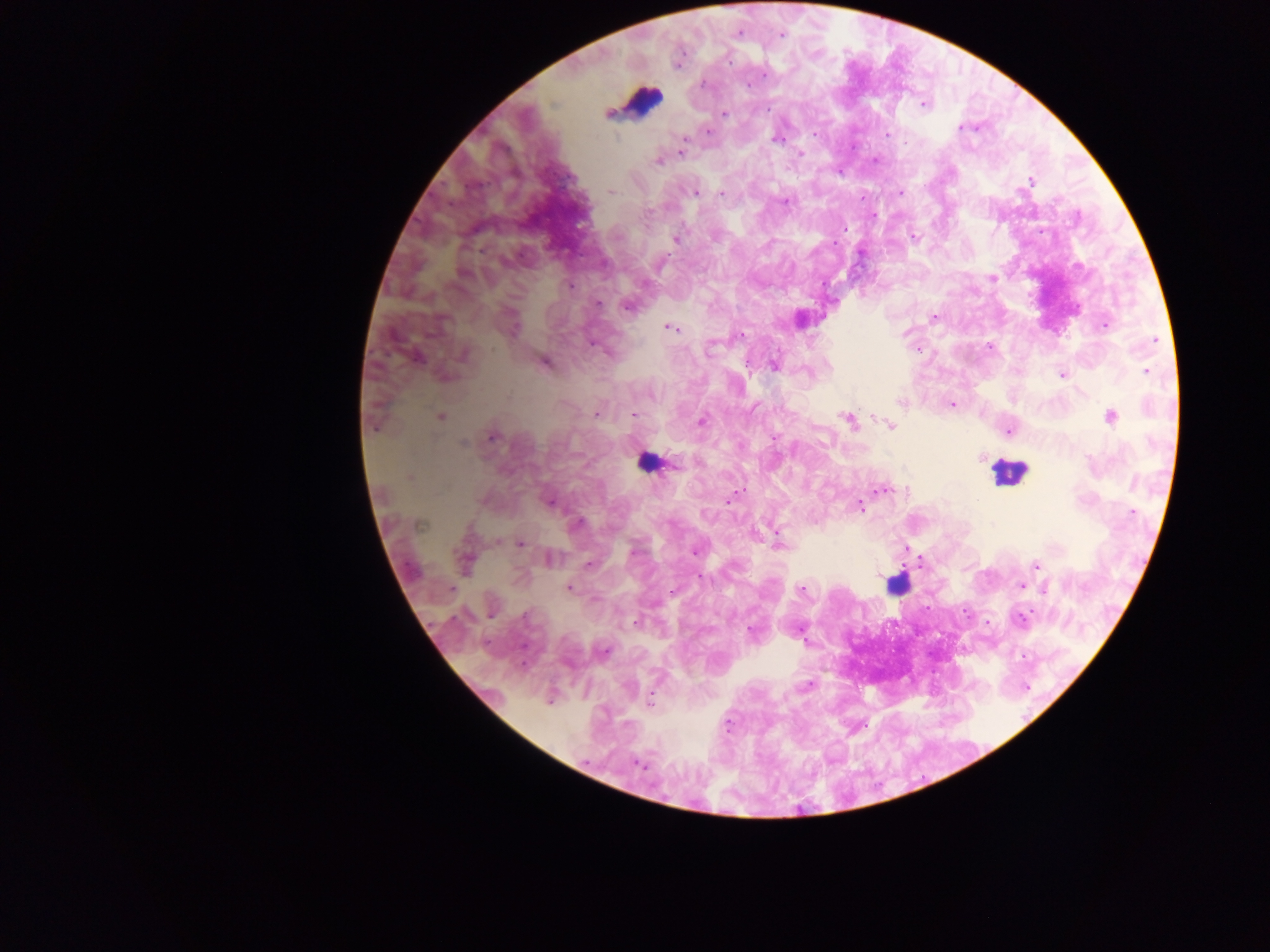
Approximate centers as [x, y] in pixels. Leukocyte locations: [643, 99], [646, 462], [1008, 472], [897, 584]. Plasmodium parasite locations: [738, 33], [781, 34], [728, 61], [704, 84], [924, 104], [768, 108], [609, 114], [724, 114], [960, 128], [709, 132], [887, 135], [777, 140], [681, 151], [800, 153], [876, 160], [658, 161], [1030, 182], [610, 191], [695, 192], [900, 192], [721, 193], [785, 201], [843, 228], [914, 237], [676, 239], [464, 274], [992, 278], [570, 286], [598, 303], [627, 307], [934, 317], [1104, 325], [513, 328], [670, 328], [741, 335], [1154, 341], [710, 347], [989, 347], [464, 355], [416, 357], [545, 363], [774, 366], [1147, 371], [1062, 374], [901, 402], [952, 405], [596, 413], [635, 415], [1110, 416], [440, 417], [848, 420], [702, 421], [891, 425], [1009, 431], [492, 437], [464, 444], [982, 457], [409, 478], [882, 490], [738, 493], [730, 500], [549, 503], [859, 506], [1133, 513], [420, 524], [578, 524], [521, 544], [780, 545], [695, 551], [550, 559], [465, 561], [589, 564], [1036, 565], [700, 577], [1020, 586], [569, 588], [1045, 588], [801, 590], [1021, 619], [636, 623], [750, 630], [801, 635], [604, 651], [806, 686], [650, 703], [640, 765]. Photographed through a microscope with a mobile-phone camera. One field of view. Image is 1270×952 pixels. Thick blood smear. Sample from Ghana.